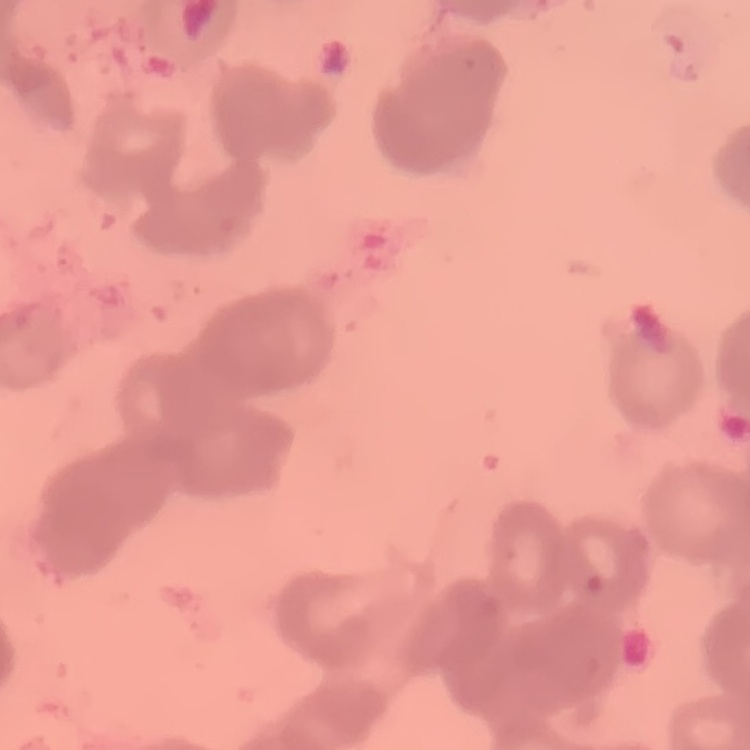

Summary:
  - Red blood cell morphology: rouleaux formation
  - Image type: square crop of a larger photomicrograph
  - Stain: Field's or Giemsa
  - Preparation: thin blood film